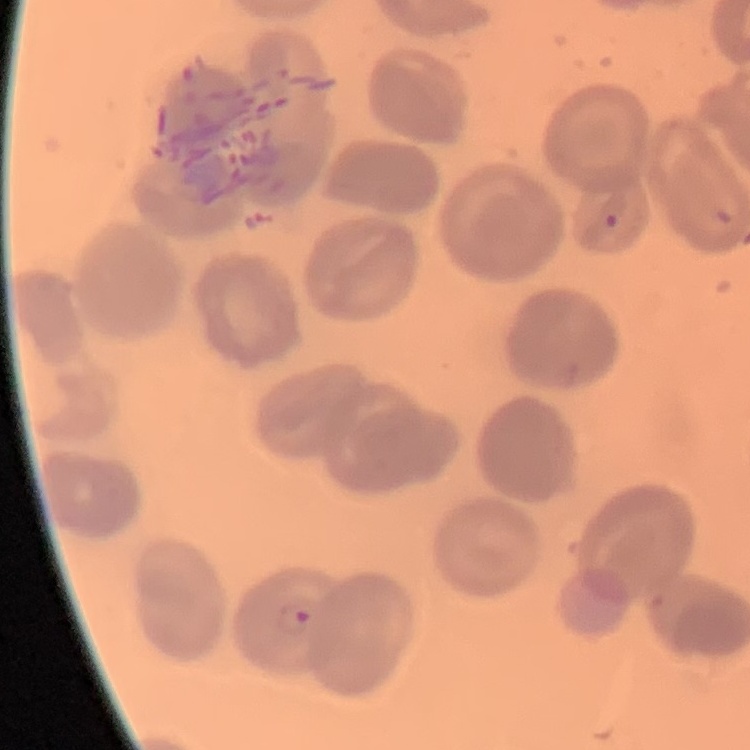 The red blood cells show no rouleaux formation. Thin peripheral smear. One tile cut from a larger photomicrograph. Field's or Giemsa stain.